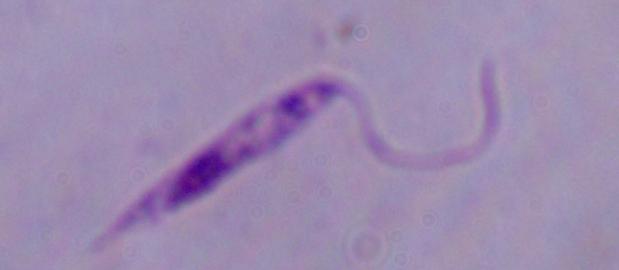
Summary:
  - Identification: Leishmania
  - Magnification: 1000x
  - Modality: photomicrograph